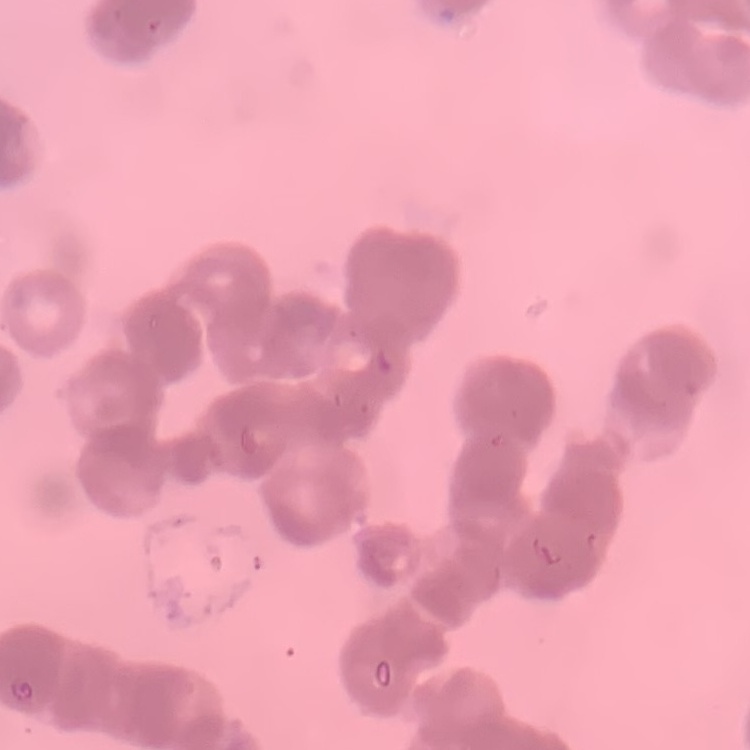
erythrocyte_morphology: rouleaux formation
preparation: thin peripheral smear
image_type: one tile cut from a larger photomicrograph
stain: Field's or Giemsa